Describe the morphology of the erythrocytes.
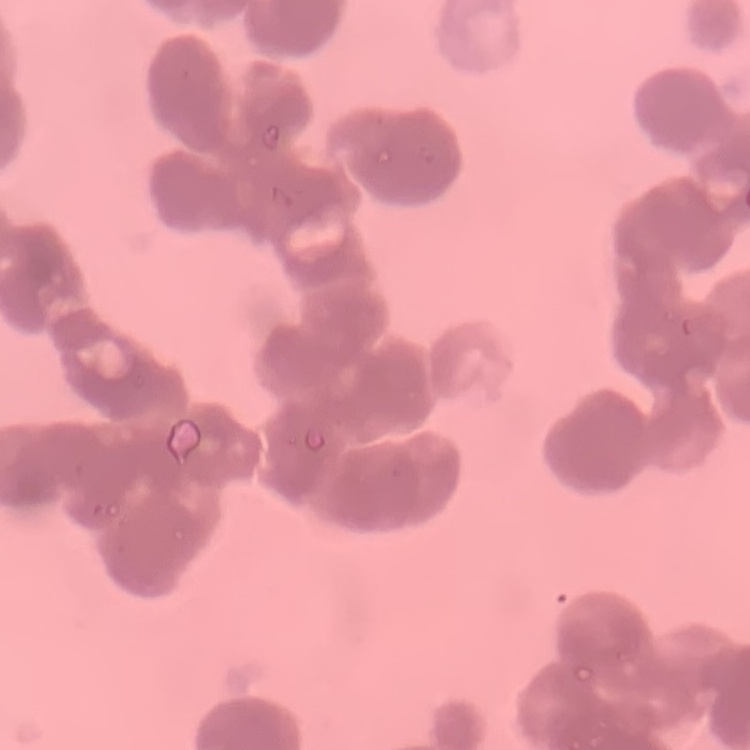

Rouleaux formation.

{
  "preparation": "thin blood film",
  "stain": "Field's or Giemsa",
  "image_type": "square crop of a larger photomicrograph"
}